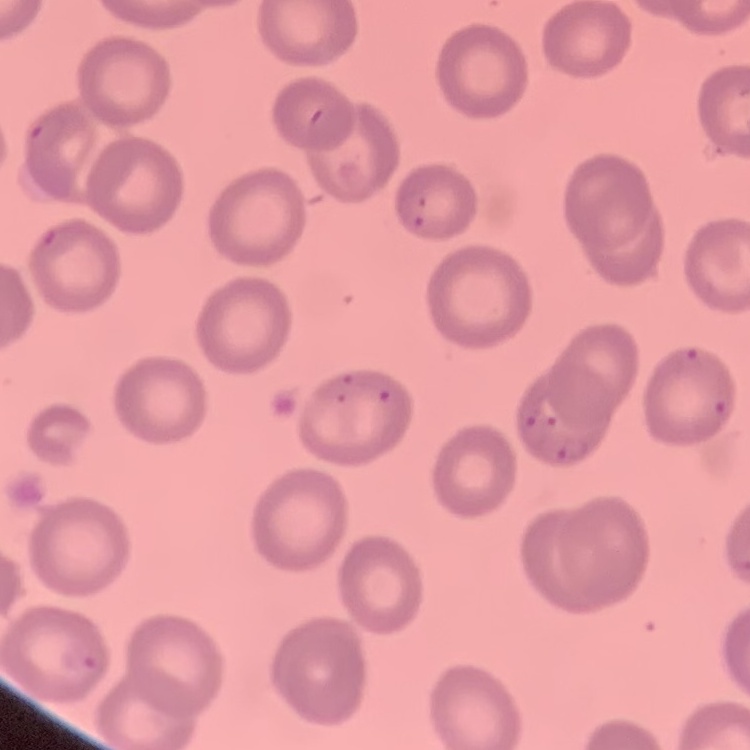

erythrocyte_morphology: no rouleaux formation
image_type: one tile cut from a larger photomicrograph
preparation: thin blood film
stain: Field's or Giemsa